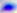

{
  "magnification": "400x",
  "modality": "photomicrograph",
  "identification": "Toxoplasma gondii"
}